Identify the blood parasite species.
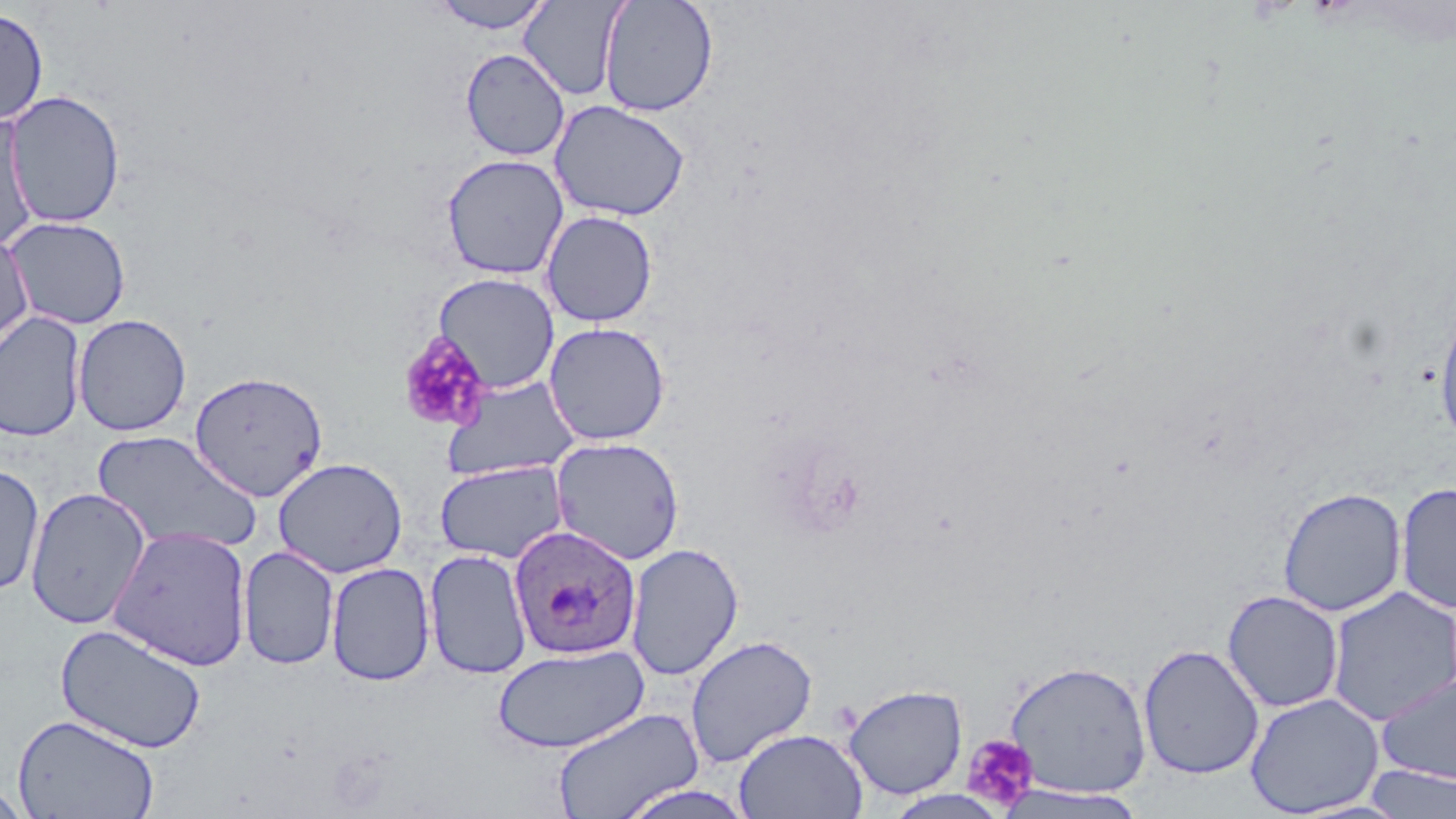
Plasmodium ovale.

Summary:
  - Coordinate format: approximate bounding boxes as (x1,y1)-(x2,y2) corner pairs in pixels
  - Platelet locations: (396,332)-(492,434), (961,734)-(1039,812)
  - Plasmodium ovale-infected red blood cell locations: (508,524)-(642,660)
  - Uninfected red blood cell locations: (426,0)-(556,33), (598,0)-(719,117), (520,1)-(625,101), (0,7)-(49,126), (460,47)-(570,161), (3,90)-(126,228), (549,99)-(691,222), (0,111)-(40,253), (441,154)-(568,279), (540,210)-(658,327), (3,216)-(132,330), (0,231)-(34,350), (433,272)-(560,393), (1434,304)-(1456,449), (0,312)-(87,443), (72,314)-(192,437), (543,322)-(671,446), (188,370)-(328,502), (441,377)-(583,481), (91,430)-(263,556), (551,437)-(685,565), (272,457)-(408,578), (434,461)-(569,564), (0,462)-(45,596), (1395,481)-(1456,614), (1276,486)-(1407,617), (25,487)-(151,629), (107,525)-(254,670), (625,542)-(744,680), (238,546)-(339,670), (424,548)-(532,679), (325,561)-(436,686), (1326,586)-(1456,726), (1222,589)-(1344,713), (54,622)-(207,753), (685,634)-(818,768), (491,642)-(650,753), (1138,644)-(1265,780), (1003,660)-(1152,798), (1377,672)-(1456,784), (843,683)-(968,800), (1244,693)-(1383,817), (552,707)-(703,819), (12,714)-(160,819), (734,727)-(867,818), (1362,765)-(1456,818), (614,782)-(759,819), (0,783)-(32,818), (995,785)-(1149,818)
  - Field of view: one of a larger specimen
  - Preparation: thin blood smear
  - Magnification: 1000x
  - Image size: 1456×819 pixels
  - Modality: optical microscopy
  - Stain: May-Grünwald-Giemsa